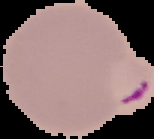
{
  "malaria_status": "parasitized",
  "preparation": "thin blood film",
  "image_size": "154×139 pixels",
  "image_type": "segmented cell region with the area outside set to black"
}